Describe the morphology of the erythrocytes.
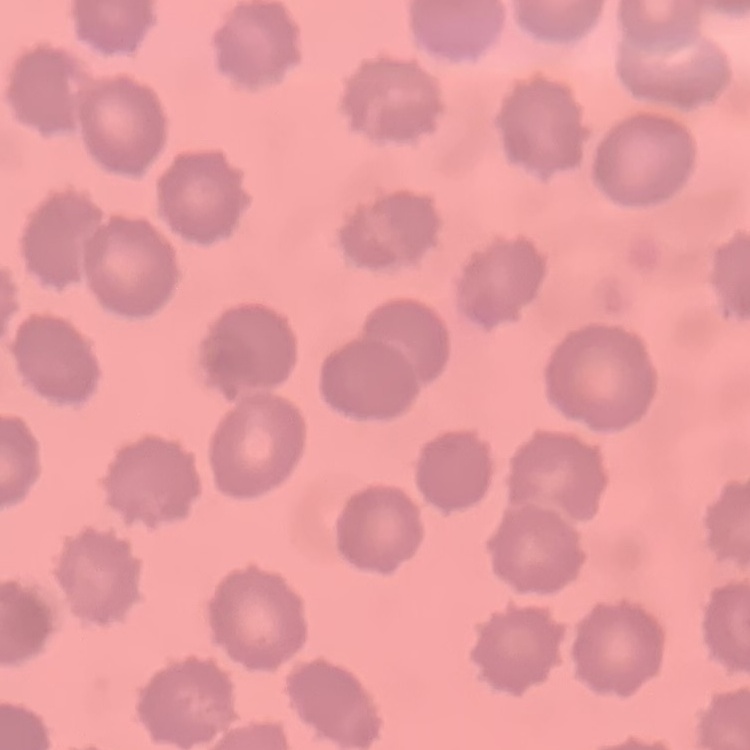

No rouleaux formation.

{
  "stain": "Field's or Giemsa",
  "image_type": "one tile cut from a larger photomicrograph",
  "preparation": "thin peripheral smear"
}